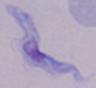
{
  "modality": "photomicrograph",
  "identification": "trypanosome",
  "magnification": "1000x"
}